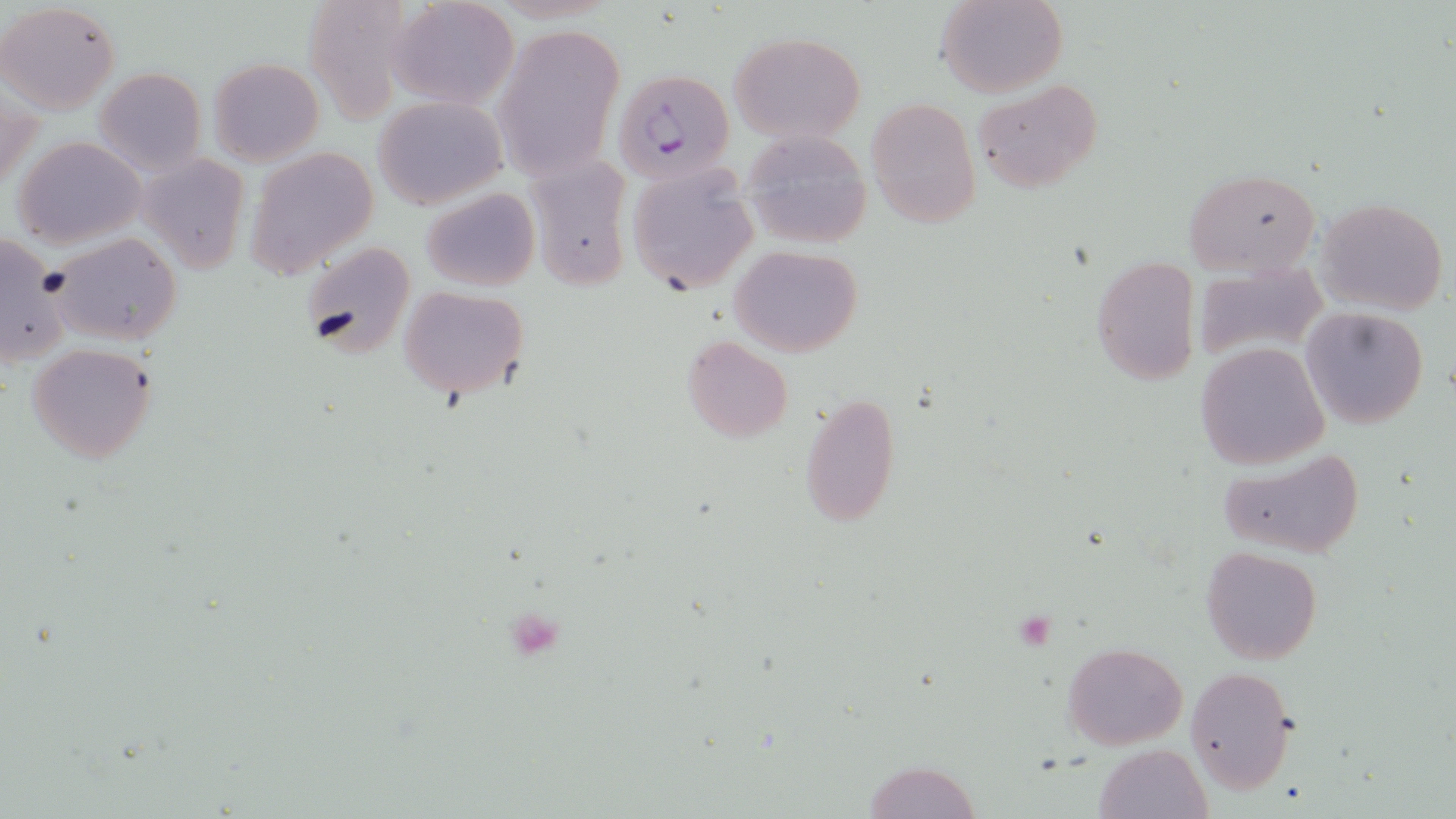
Summary:
  - Coordinate format: approximate bounding boxes as (x1, y1, x2, y2) in pixels
  - Uninfected red blood cell locations: (391, 0, 520, 110), (937, 0, 1066, 98), (0, 1, 121, 116), (303, 1, 411, 123), (493, 24, 624, 181), (727, 30, 867, 145), (208, 57, 323, 165), (95, 67, 207, 175), (974, 79, 1103, 193), (373, 95, 508, 209), (866, 98, 979, 227), (741, 129, 874, 248), (13, 136, 148, 248), (246, 147, 379, 280), (522, 151, 634, 291), (139, 154, 251, 274), (626, 165, 759, 296), (1184, 168, 1321, 276), (421, 187, 540, 292), (1316, 198, 1449, 315), (1, 231, 68, 368), (48, 232, 183, 347), (299, 241, 417, 363), (729, 244, 863, 356), (1091, 257, 1201, 385), (1194, 261, 1329, 365), (398, 285, 528, 398), (1301, 306, 1429, 429), (681, 336, 794, 442), (1196, 342, 1329, 470), (27, 343, 159, 464), (797, 390, 899, 529), (1214, 447, 1364, 559), (1200, 546, 1322, 663), (1062, 642, 1186, 749), (1186, 665, 1297, 794), (1093, 743, 1211, 819), (862, 759, 984, 818)
  - Platelet locations: (1018, 611, 1055, 650), (515, 613, 560, 662)
  - Plasmodium falciparum-infected red blood cell locations: (613, 69, 734, 186)
  - Slide-level diagnosis: Plasmodium falciparum
  - Stain: May-Grünwald-Giemsa
  - Preparation: thin blood smear
  - Modality: optical microscopy
  - Image size: 1456×819 pixels
  - Field of view: one of a larger specimen
  - Magnification: 1000x